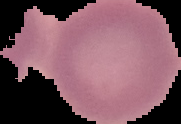

Summary:
  - Image size: 181×124 pixels
  - Image type: segmented cell region with the area outside set to black
  - Preparation: thin blood film
  - Malaria status: uninfected